Give the position of every leukocyte visible.
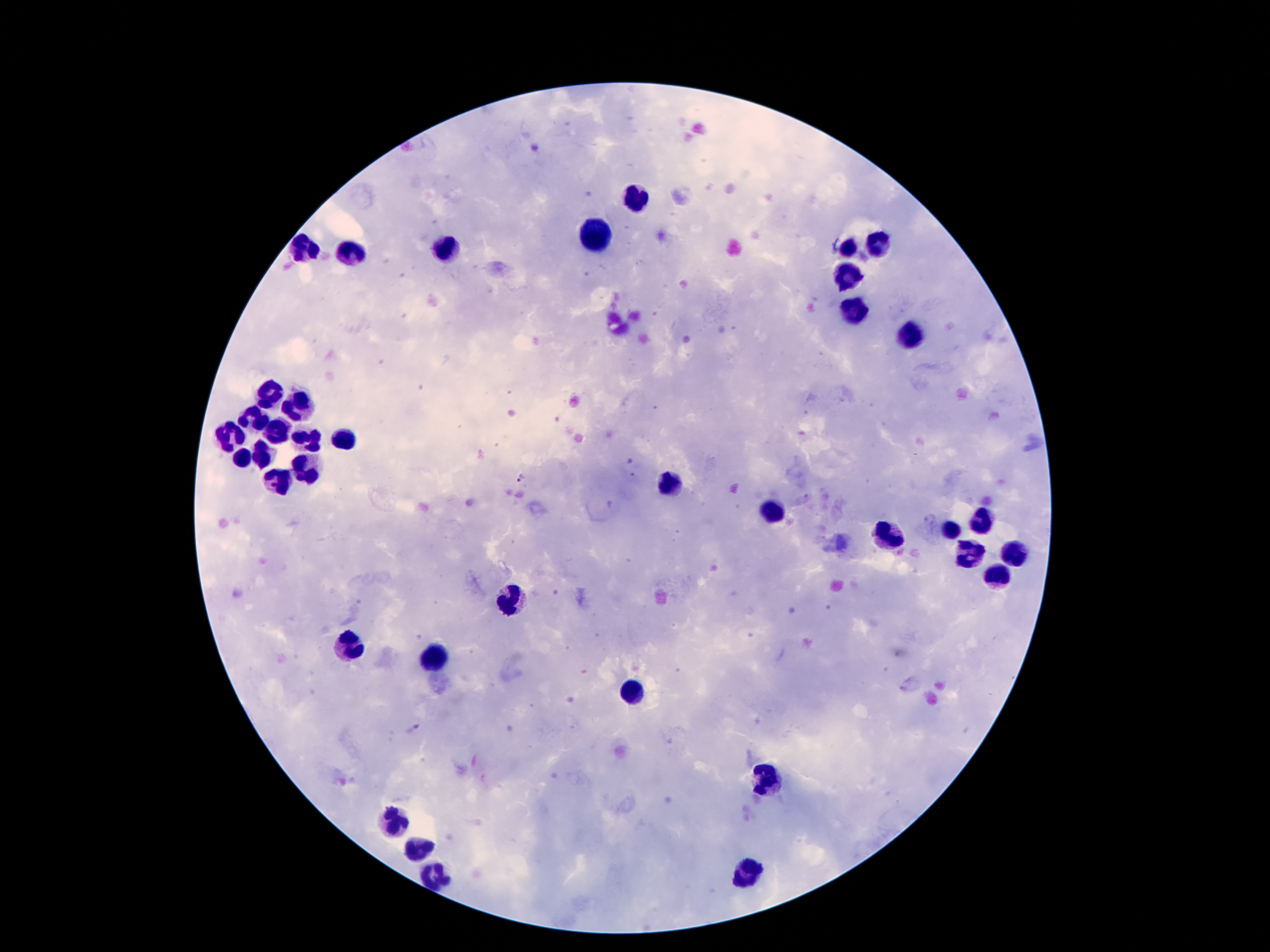

Approximate centers as {x, y} in pixels.
Leukocytes: {637, 194}, {598, 233}, {877, 242}, {446, 248}, {848, 248}, {303, 249}, {348, 256}, {852, 270}, {859, 310}, {911, 335}, {271, 390}, {301, 407}, {257, 417}, {232, 431}, {284, 436}, {344, 440}, {307, 442}, {264, 452}, {239, 460}, {310, 470}, {280, 485}, {666, 485}, {768, 515}, {980, 520}, {948, 532}, {888, 536}, {1016, 554}, {972, 556}, {997, 576}, {512, 596}, {350, 646}, {434, 658}, {634, 689}, {771, 778}, {396, 821}, {418, 844}, {752, 869}, {437, 876}.

Malaria parasite locations: {521, 476}. Thick peripheral-blood smear. Giemsa stain. 100x magnification. Smartphone photograph taken through the microscope eyepiece. Image is 1270×952 pixels. One field from this slide. Patient malaria status: infected with Plasmodium falciparum.